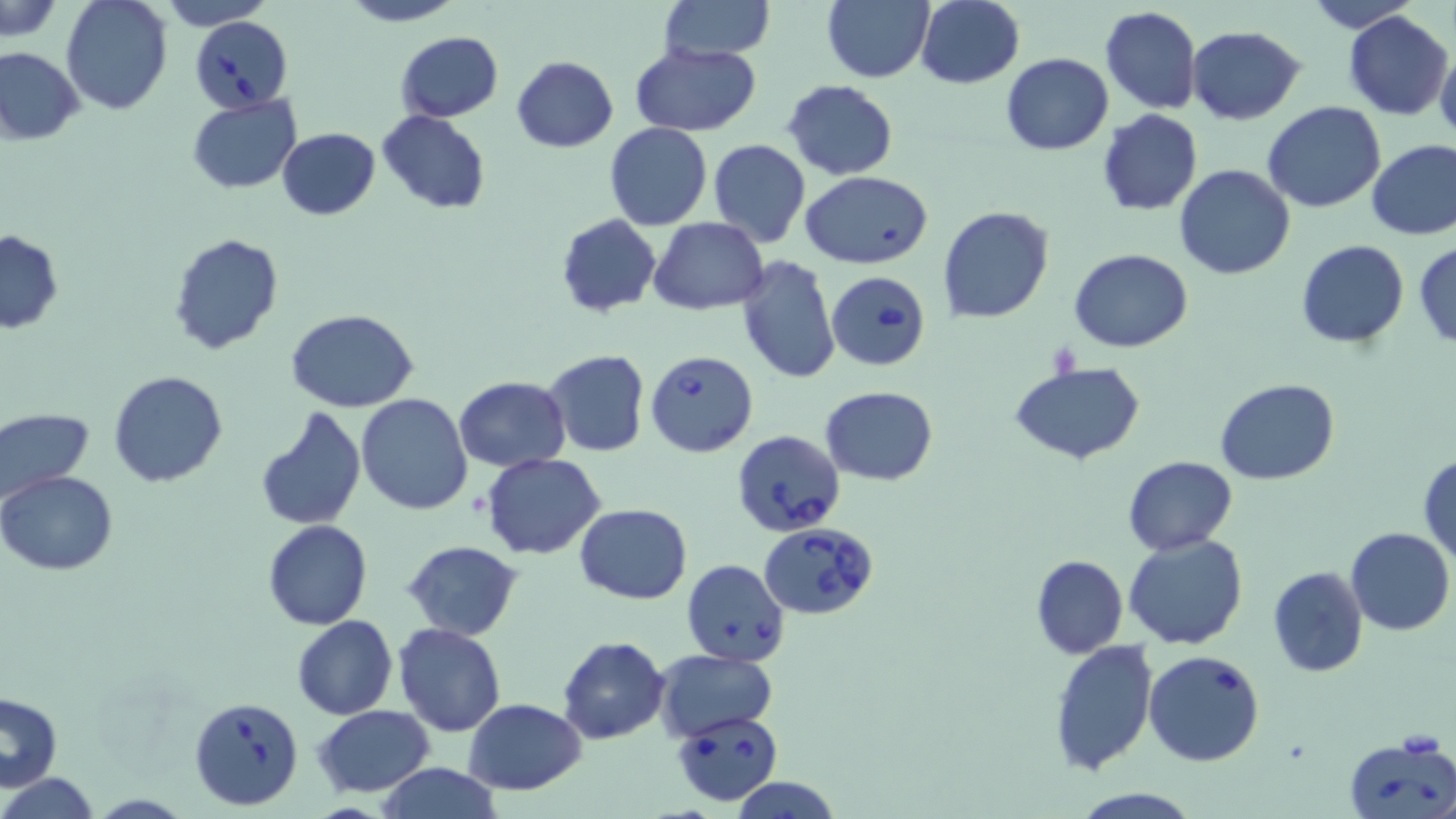
Summary:
  - Coordinate format: approximate bounding boxes as (x1, y1, x2, y2) in pixels
  - Uninfected red blood cell locations: (1, 0, 65, 39), (61, 0, 173, 115), (159, 0, 276, 29), (339, 0, 464, 26), (1302, 0, 1421, 33), (659, 1, 775, 63), (823, 1, 933, 82), (915, 1, 1024, 88), (1100, 6, 1202, 114), (1343, 11, 1454, 120), (1187, 25, 1307, 123), (395, 32, 504, 121), (630, 41, 763, 136), (1435, 45, 1456, 146), (0, 48, 84, 145), (1001, 52, 1113, 155), (511, 55, 618, 152), (782, 80, 899, 181), (187, 95, 301, 193), (1262, 102, 1386, 214), (1096, 109, 1203, 215), (376, 110, 490, 213), (604, 123, 712, 231), (277, 127, 380, 219), (1366, 139, 1456, 239), (709, 140, 811, 248), (1173, 164, 1294, 280), (799, 170, 934, 269), (937, 206, 1054, 325), (556, 214, 662, 317), (650, 216, 769, 313), (0, 231, 64, 333), (168, 234, 284, 355), (1297, 239, 1410, 347), (1414, 239, 1456, 347), (1069, 247, 1193, 354), (736, 256, 841, 386), (286, 308, 418, 414), (543, 350, 650, 456), (1010, 361, 1145, 464), (108, 370, 229, 489), (453, 377, 572, 471), (1215, 379, 1341, 486), (821, 385, 939, 485), (356, 392, 473, 514), (0, 406, 95, 505), (253, 406, 367, 530), (1418, 452, 1456, 564), (481, 453, 605, 560), (1122, 455, 1237, 555), (0, 470, 119, 576), (574, 503, 692, 602), (263, 520, 372, 630), (1345, 526, 1455, 635), (1122, 533, 1249, 650), (402, 540, 522, 640), (1030, 554, 1127, 658), (1268, 566, 1369, 677), (291, 615, 397, 720), (393, 623, 505, 737), (558, 636, 670, 744), (1049, 640, 1159, 774), (655, 649, 777, 739), (1143, 649, 1266, 767), (1, 692, 63, 790), (463, 698, 585, 795), (312, 705, 437, 796), (374, 763, 503, 819), (2, 773, 100, 818), (729, 776, 843, 818), (1069, 788, 1203, 819)
  - Babesia divergens-infected red blood cell locations: (191, 15, 292, 112), (826, 271, 930, 371), (645, 350, 758, 457), (731, 430, 846, 536), (760, 523, 879, 620), (683, 560, 788, 665), (189, 695, 305, 809), (671, 711, 784, 806), (1344, 735, 1456, 818)
  - Slide-level diagnosis: Babesia divergens
  - Magnification: 1000x
  - Modality: optical microscopy
  - Stain: May-Grünwald-Giemsa
  - Field of view: one of a larger specimen
  - Preparation: thin blood smear
  - Image size: 1456×819 pixels